Assess the morphology of the red blood cells.
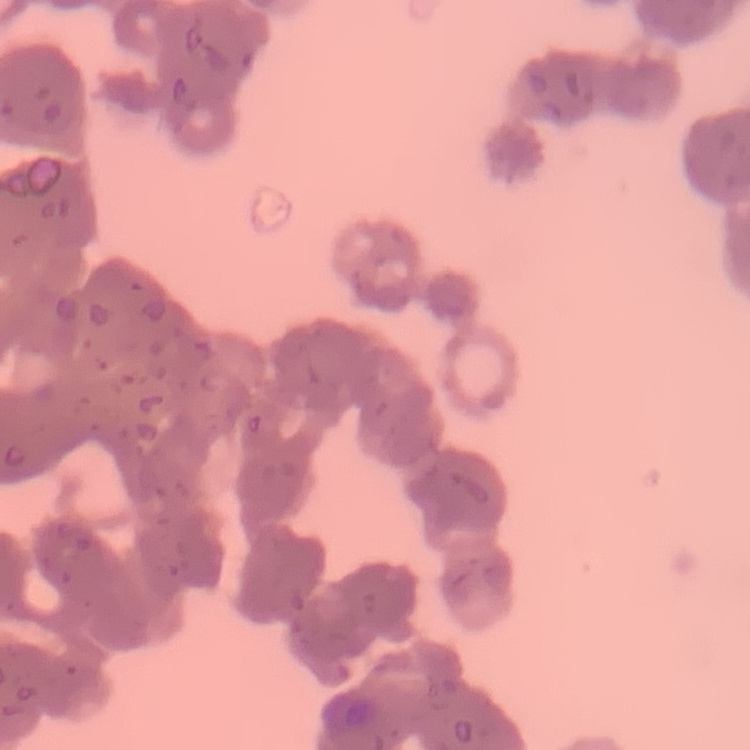

They show rouleaux formation.

image type = square crop of a larger photomicrograph
stain = Field's or Giemsa
preparation = thin peripheral smear